Locate and identify every blood parasite.
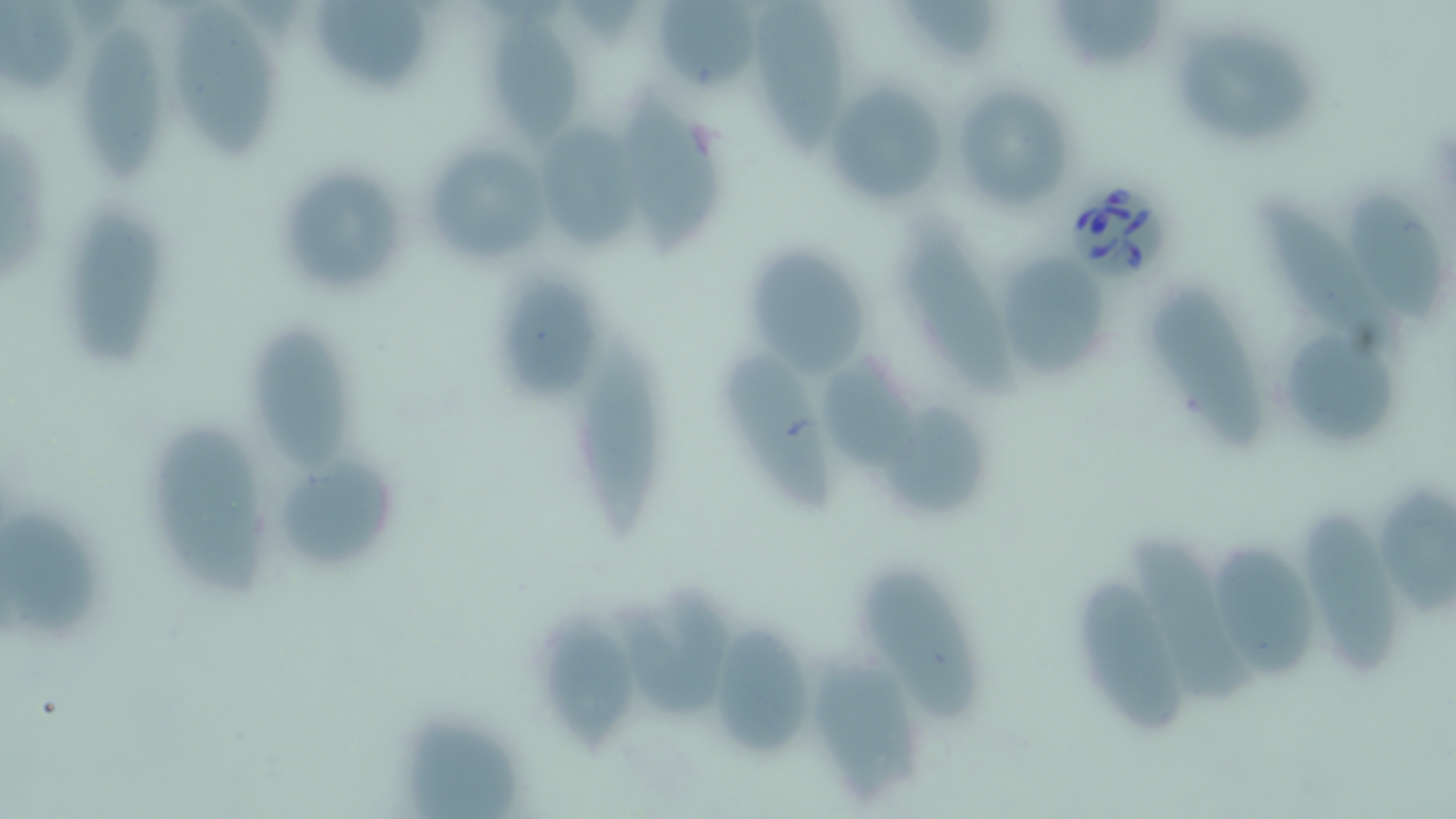
Approximate bounding boxes as [x1, y1, x2, y2] in pixels.
Babesia divergens-infected red blood cells: [1067, 175, 1170, 280].
No Plasmodium falciparum, Plasmodium ovale, Plasmodium malariae, Plasmodium vivax, or Trypanosoma brucei observed.

slide-level diagnosis = Babesia divergens
uninfected red blood cell locations = approximate bounding boxes as [x1, y1, x2, y2] in pixels: [169, 0, 278, 161], [314, 0, 432, 94], [653, 0, 754, 92], [749, 0, 847, 159], [896, 0, 996, 61], [1049, 0, 1168, 69], [0, 1, 75, 92], [485, 10, 580, 146], [78, 20, 167, 183], [1174, 26, 1317, 141], [824, 82, 950, 206], [949, 83, 1075, 213], [621, 94, 722, 262], [534, 124, 643, 256], [421, 138, 554, 270], [287, 165, 404, 296], [1255, 185, 1390, 345], [1351, 187, 1447, 328], [65, 194, 167, 370], [894, 216, 1028, 404], [750, 246, 872, 380], [1007, 246, 1109, 381], [494, 269, 600, 398], [1148, 285, 1273, 449], [252, 321, 350, 475], [1280, 329, 1397, 443], [579, 341, 660, 543], [725, 342, 840, 513], [818, 351, 922, 471], [884, 395, 986, 519], [151, 418, 270, 603], [281, 451, 403, 570], [1379, 475, 1456, 623], [1302, 503, 1394, 679], [0, 510, 99, 642], [1131, 531, 1258, 701], [1212, 536, 1320, 683], [861, 565, 983, 725], [1080, 574, 1189, 738], [620, 580, 741, 722], [534, 602, 627, 753], [712, 620, 813, 757], [803, 653, 926, 803], [401, 712, 525, 817]
preparation = thin blood smear
stain = May-Grünwald-Giemsa
field of view = single
magnification = 1000x
modality = light microscopy
image size = 1456×819 pixels